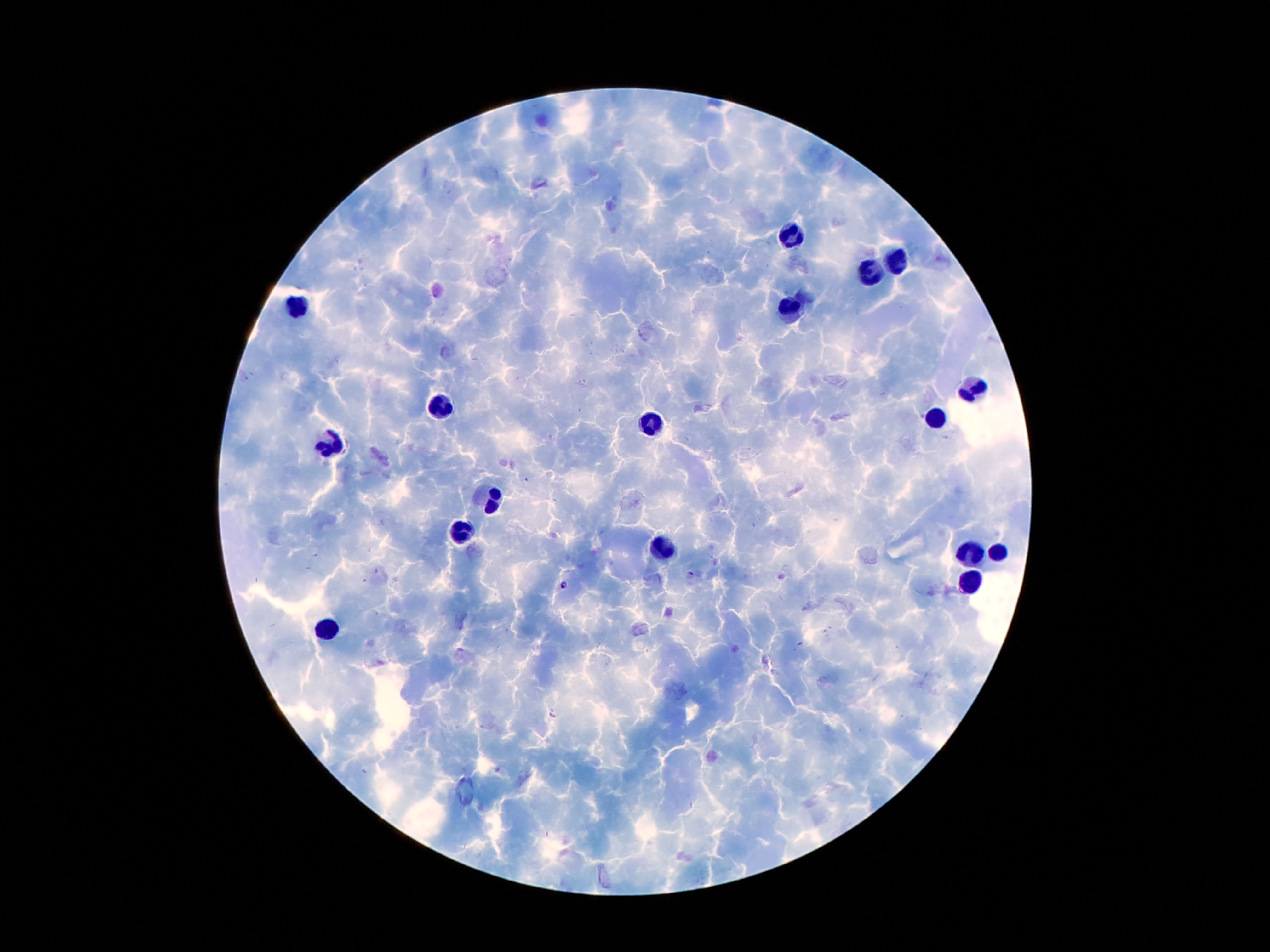
Approximate centers as [x, y] in pixels. Plasmodium parasite locations: [691, 573], [563, 585]. Leukocyte locations: [792, 233], [895, 260], [872, 272], [298, 308], [790, 312], [974, 384], [441, 403], [934, 417], [647, 424], [328, 445], [491, 499], [460, 535], [664, 546], [972, 552], [997, 554], [970, 583], [328, 628]. Thick blood film. Single field of view. 100x magnification. Image is 1270×952 pixels. Giemsa-stained preparation. Patient malaria status: infected with Plasmodium falciparum. Smartphone photograph taken through the microscope eyepiece.